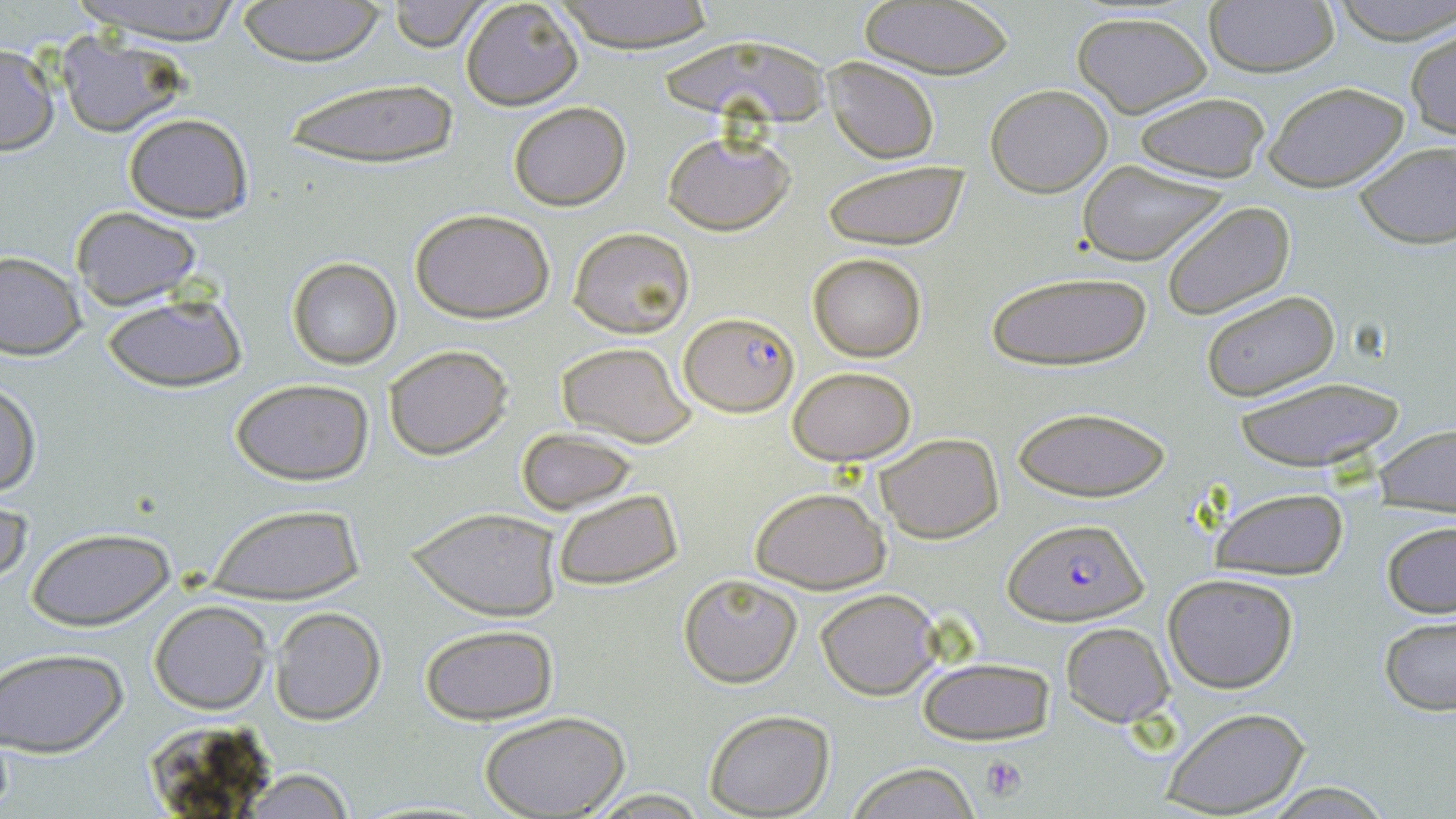

Summary:
  - Coordinate format: approximate bounding boxes as [x1, y1, x2, y2] in pixels
  - Plasmodium falciparum-infected red blood cell locations: [681, 312, 799, 416], [1004, 518, 1149, 627]
  - Uninfected red blood cell locations: [71, 0, 249, 45], [234, 0, 387, 66], [389, 0, 488, 51], [552, 0, 718, 54], [858, 0, 1017, 81], [1331, 0, 1456, 44], [459, 1, 584, 110], [1201, 1, 1340, 77], [1072, 12, 1212, 117], [1406, 28, 1455, 140], [55, 31, 188, 137], [655, 35, 835, 133], [0, 43, 59, 155], [824, 58, 939, 163], [276, 74, 467, 173], [1262, 81, 1407, 191], [986, 84, 1113, 196], [1132, 91, 1273, 183], [507, 101, 631, 210], [122, 112, 254, 223], [663, 132, 793, 236], [1353, 143, 1456, 249], [1075, 160, 1233, 264], [822, 161, 969, 252], [1161, 201, 1295, 319], [70, 207, 202, 309], [408, 208, 557, 323], [568, 226, 695, 338], [0, 251, 86, 360], [808, 253, 927, 362], [286, 257, 401, 369], [985, 270, 1151, 372], [1198, 289, 1343, 404], [102, 292, 248, 393], [555, 342, 698, 448], [382, 345, 511, 460], [788, 366, 916, 465], [1228, 375, 1409, 472], [1, 378, 39, 499], [230, 379, 376, 486], [1010, 404, 1171, 503], [1375, 424, 1456, 516], [518, 429, 639, 514], [874, 432, 1004, 543], [750, 486, 891, 593], [1210, 486, 1351, 580], [552, 488, 682, 590], [1, 493, 31, 594], [203, 503, 363, 600], [407, 506, 563, 621], [1381, 519, 1456, 619], [26, 526, 174, 630], [1162, 572, 1299, 693], [679, 573, 803, 687], [814, 586, 943, 699], [149, 601, 271, 714], [269, 606, 387, 725], [1380, 618, 1456, 714], [1060, 621, 1172, 726], [421, 625, 559, 725], [1, 650, 126, 756], [917, 657, 1053, 745], [1161, 706, 1309, 818], [703, 710, 835, 817], [481, 712, 628, 819], [143, 716, 277, 809], [846, 764, 980, 819], [237, 769, 357, 819], [1257, 783, 1399, 816]
  - Platelet locations: [982, 755, 1027, 800]
  - Slide-level diagnosis: Plasmodium falciparum
  - Field of view: single
  - Modality: light microscopy
  - Magnification: 1000x
  - Preparation: thin blood smear
  - Stain: May-Grünwald-Giemsa
  - Image size: 1456×819 pixels